Locate every malaria parasite.
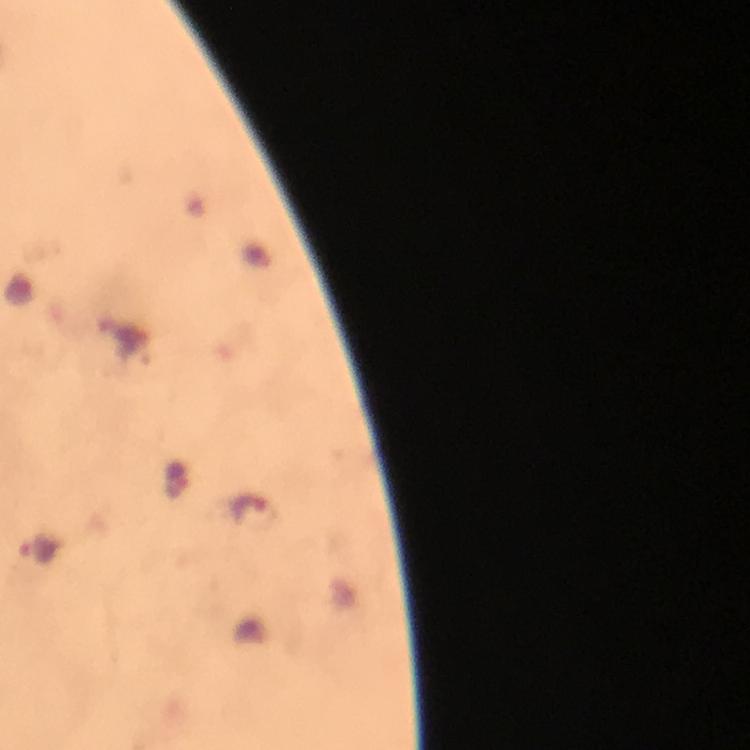

Approximate centers as (x, y) in pixels.
Malaria parasites: (178, 479), (248, 508), (39, 547).

Giemsa-stained preparation. Image is 750×750 pixels. Smartphone photograph taken through a microscope. A crop from one field of view. Thick blood smear. Immersion oil was used. From a malaria diagnostic workup. At 100x magnification.